Report the malaria status of this cell.
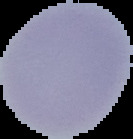
Uninfected.

Segmented cell region on a black background. Image is 133×139 pixels. From a thin blood film.